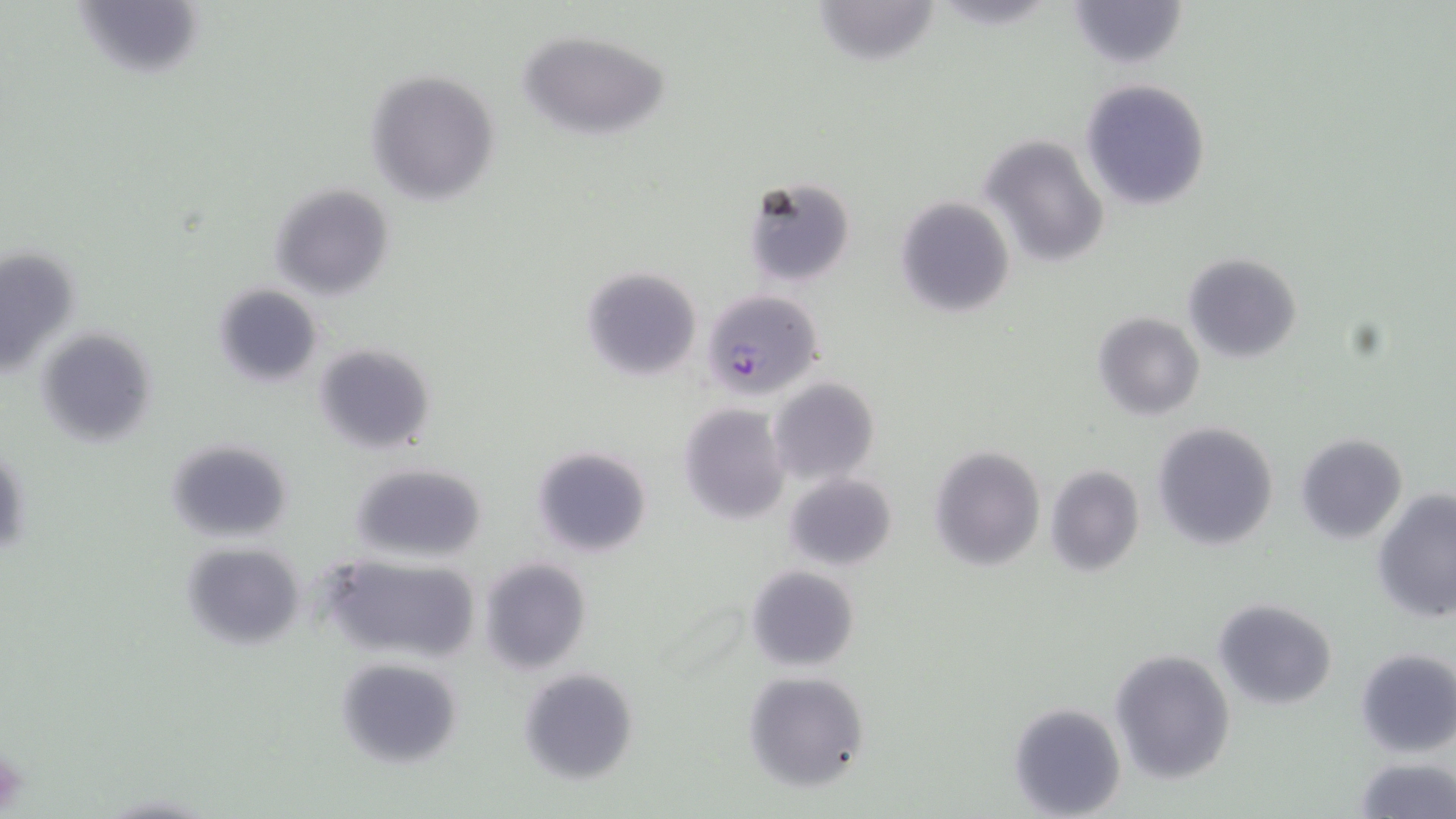
Summary:
  - Coordinate format: approximate bounding boxes as (x1, y1, x2, y2) in pixels
  - Plasmodium falciparum-infected red blood cell locations: (699, 288, 824, 397)
  - Platelet locations: (0, 748, 27, 815)
  - Uninfected red blood cell locations: (811, 0, 944, 67), (1065, 0, 1189, 71), (518, 28, 670, 140), (362, 69, 500, 206), (1081, 78, 1210, 210), (980, 135, 1110, 270), (741, 178, 856, 289), (270, 183, 395, 301), (895, 195, 1015, 318), (0, 245, 84, 382), (1181, 253, 1304, 361), (579, 267, 702, 381), (212, 284, 324, 387), (1093, 312, 1205, 421), (36, 324, 158, 446), (313, 341, 437, 454), (769, 377, 879, 484), (680, 404, 791, 524), (1151, 420, 1279, 551), (1294, 433, 1408, 543), (165, 437, 296, 542), (531, 445, 653, 557), (928, 445, 1046, 571), (348, 461, 488, 564), (1044, 465, 1145, 575), (783, 472, 898, 570), (1372, 490, 1456, 627), (180, 541, 307, 652), (321, 553, 483, 664), (477, 557, 592, 676), (745, 565, 860, 673), (1213, 598, 1337, 709), (1109, 648, 1236, 784), (1354, 649, 1456, 757), (334, 656, 463, 768), (517, 667, 638, 785), (743, 669, 869, 791), (1008, 701, 1127, 818), (1350, 759, 1456, 817)
  - Slide-level diagnosis: Plasmodium falciparum
  - Magnification: 1000x
  - Image size: 1456×819 pixels
  - Stain: May-Grünwald-Giemsa
  - Modality: light microscopy
  - Field of view: one of a larger specimen
  - Preparation: thin blood film